Comment on the morphology of the erythrocytes.
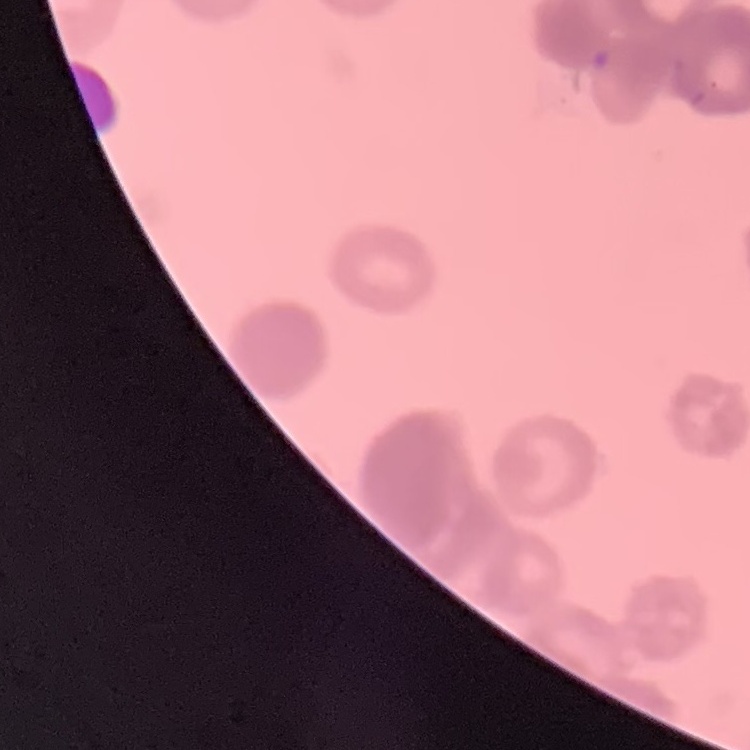
Rouleaux formation.

image type = square crop of a larger photomicrograph
preparation = thin blood film
stain = Field's or Giemsa